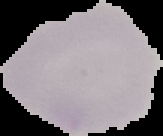
result: no Plasmodium parasites seen
preparation: thin blood film
image_type: segmented cell region with the area outside set to black
image_size: 163×136 pixels